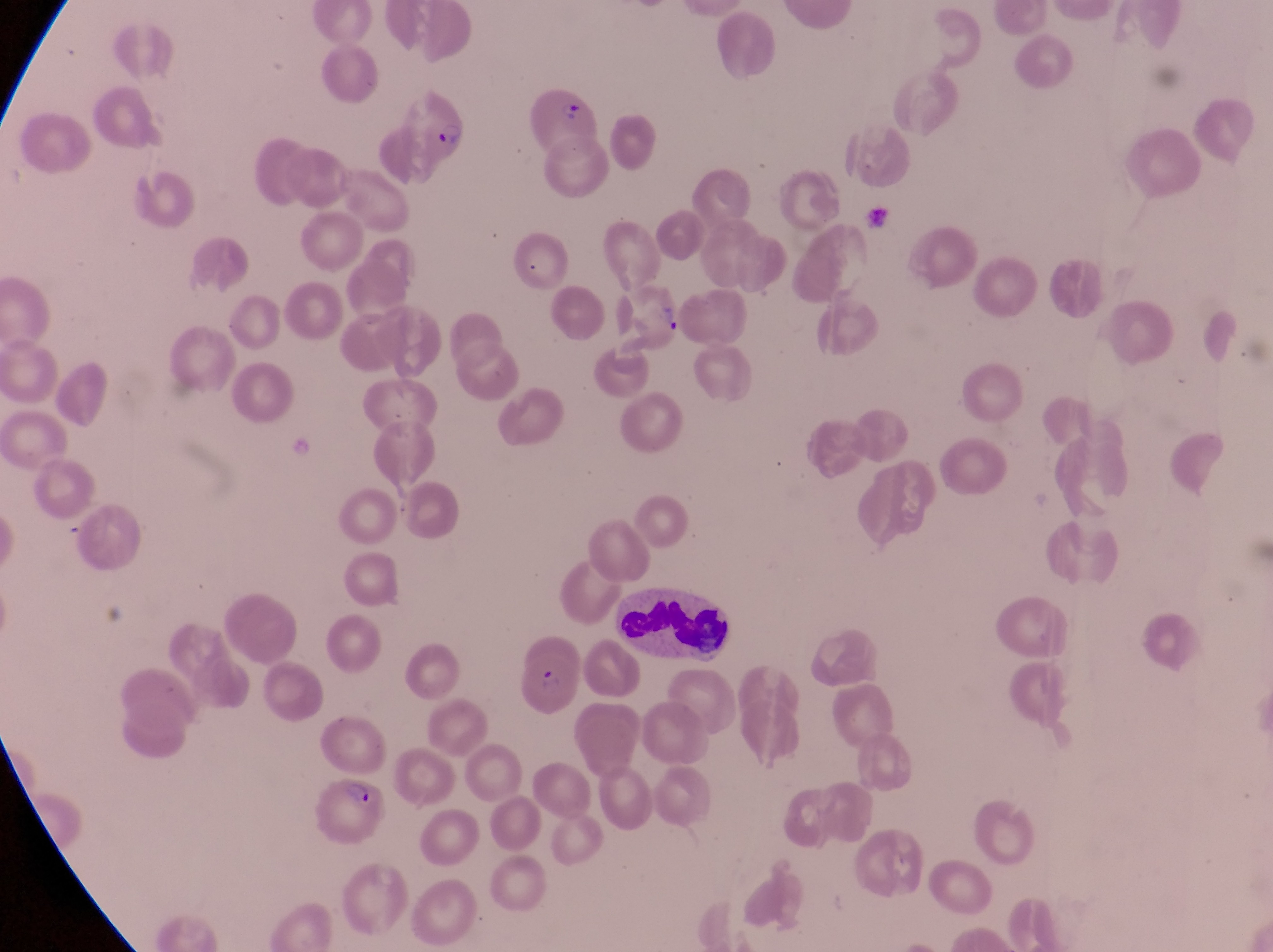
preparation = thin blood film
parasitised red blood cell locations = approximate bounding boxes as left top right bottom in pixels: 526 85 601 165; 400 92 472 167; 614 282 688 354; 512 631 581 718; 310 772 387 846
field of view = single
country = Uganda
image size = 1273×952 pixels
leukocyte locations = approximate bounding boxes as left top right bottom in pixels: 609 584 729 669
capture = smartphone photograph through the eyepiece of an Olympus CX-23 microscope
magnification = 1000x